Assess the morphology of the erythrocytes.
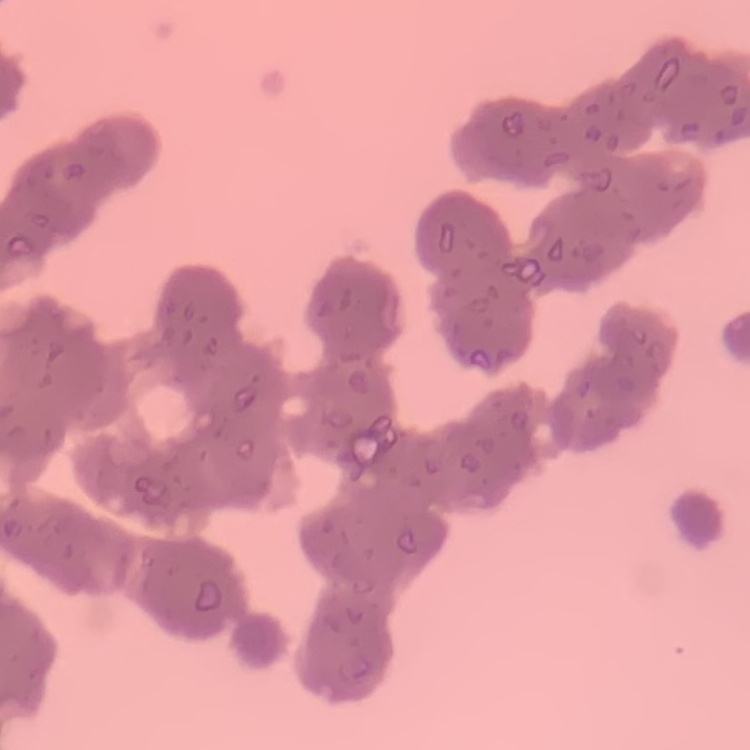

They show rouleaux formation.

Thin blood smear. Square crop of a larger photomicrograph. Stained with either Field's or Giemsa.